Identify the parasite.
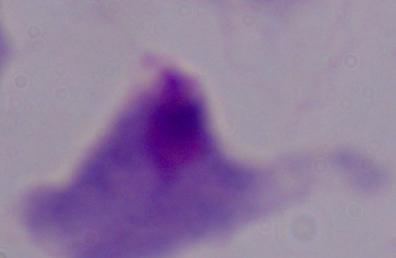

This is a trichomonad.

Photomicrograph. 1000x magnification.